Give the position of every leukocyte visible.
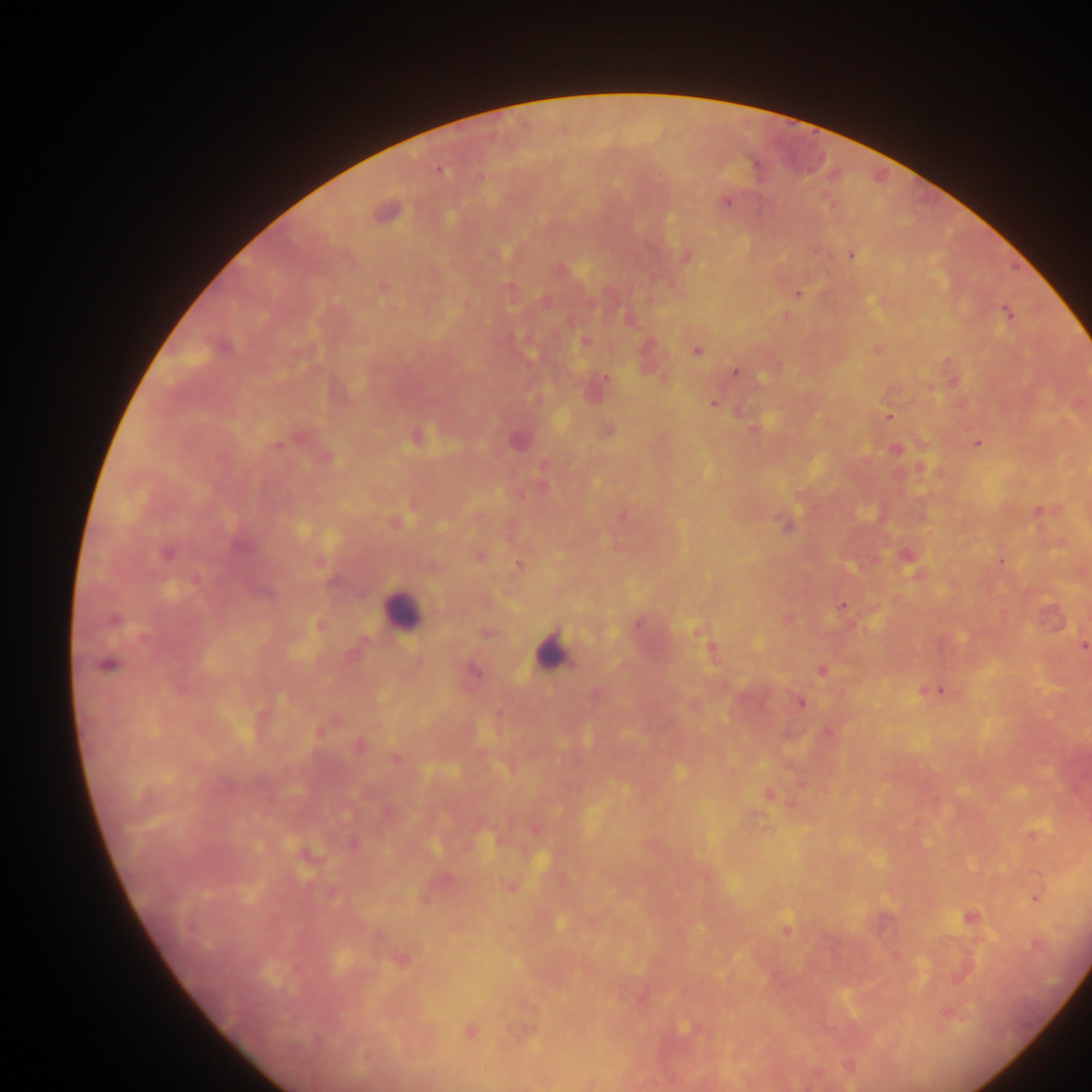
Approximate centers as (x, y) in pixels.
Leukocytes: (401, 610), (550, 652).

Plasmodium parasite locations: (756, 165), (439, 171), (727, 202), (384, 213), (851, 254), (685, 258), (383, 287), (510, 288), (798, 294), (1007, 312), (585, 342), (696, 351), (736, 372), (605, 377), (713, 403), (888, 416), (608, 430), (416, 437), (517, 441), (978, 443), (278, 445), (786, 525), (240, 547), (166, 554), (479, 555), (518, 565), (842, 607), (114, 619), (637, 624), (1083, 646), (711, 649), (108, 665), (822, 670), (474, 671), (940, 691), (800, 703), (358, 745), (394, 758), (769, 795), (498, 840), (1036, 897), (970, 917), (560, 923), (786, 928), (684, 1028), (469, 1032). Image is 1092×1092 pixels. One field of view. Sample from Ghana. Thick blood smear. Photographed through a microscope with a mobile-phone camera.